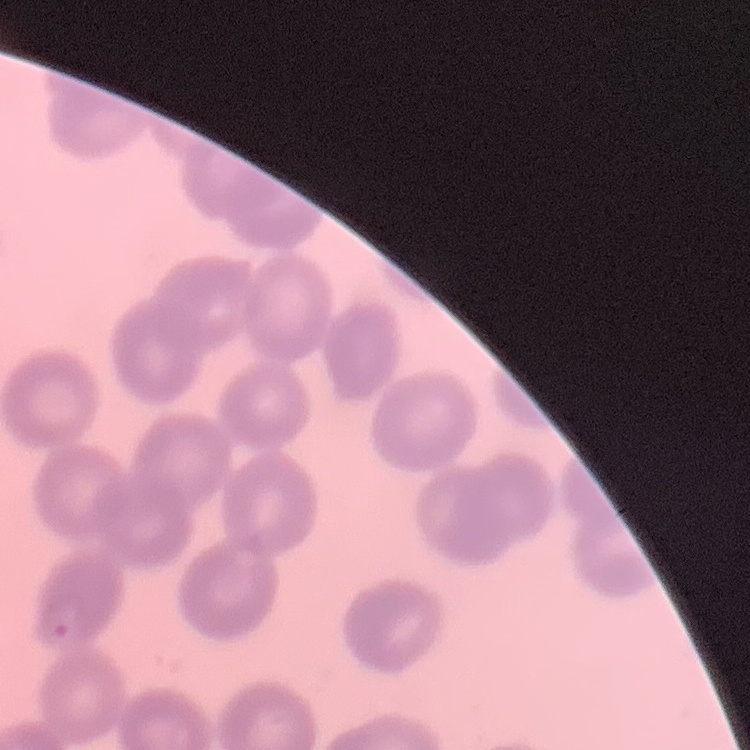
The red blood cells show no rouleaux formation. Field's or Giemsa stain. Thin peripheral smear. One tile cut from a larger photomicrograph.